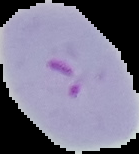

result = malaria parasites identified
image type = segmented cell region with the area outside set to black
preparation = thin blood smear
image size = 139×154 pixels